Comment on the morphology of the erythrocytes.
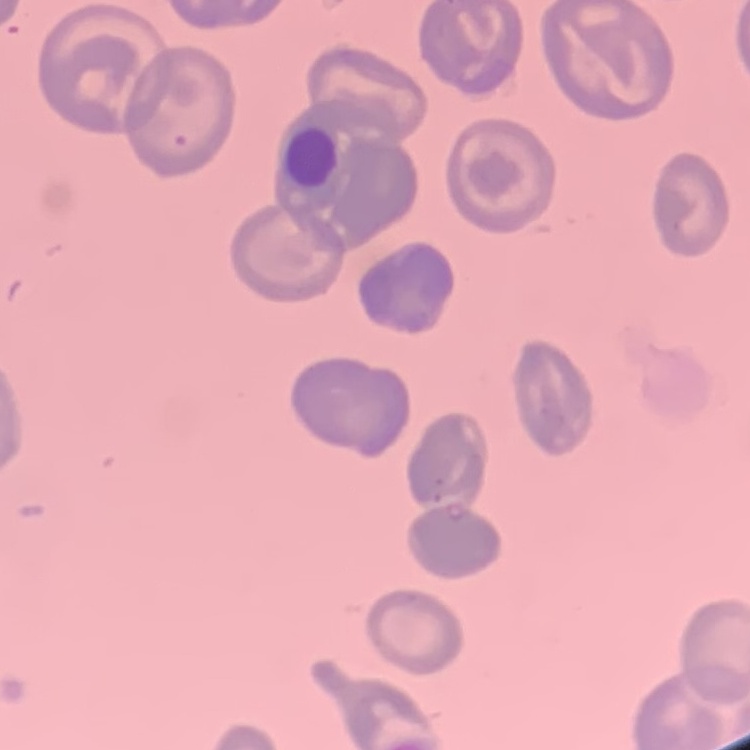
They show no rouleaux formation.

Thin blood film. Square crop of a larger photomicrograph. Field's or Giemsa stain.